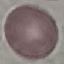
Summary:
  - Malaria status: uninfected
  - Stain: Giemsa
  - Capture: smartphone camera at the microscope eyepiece
  - Image type: automatically extracted cell patch, resized to 64 × 64 pixels
  - Preparation: thin smear